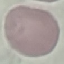
malaria_status: uninfected
image_type: automatically extracted cell patch, resized to 64 × 64 pixels
preparation: thin blood smear
capture: smartphone through the microscope eyepiece
stain: Giemsa